Identify the cell.
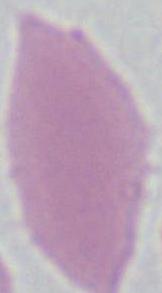
An erythrocyte.

Summary:
  - Modality: photomicrograph
  - Magnification: 1000x